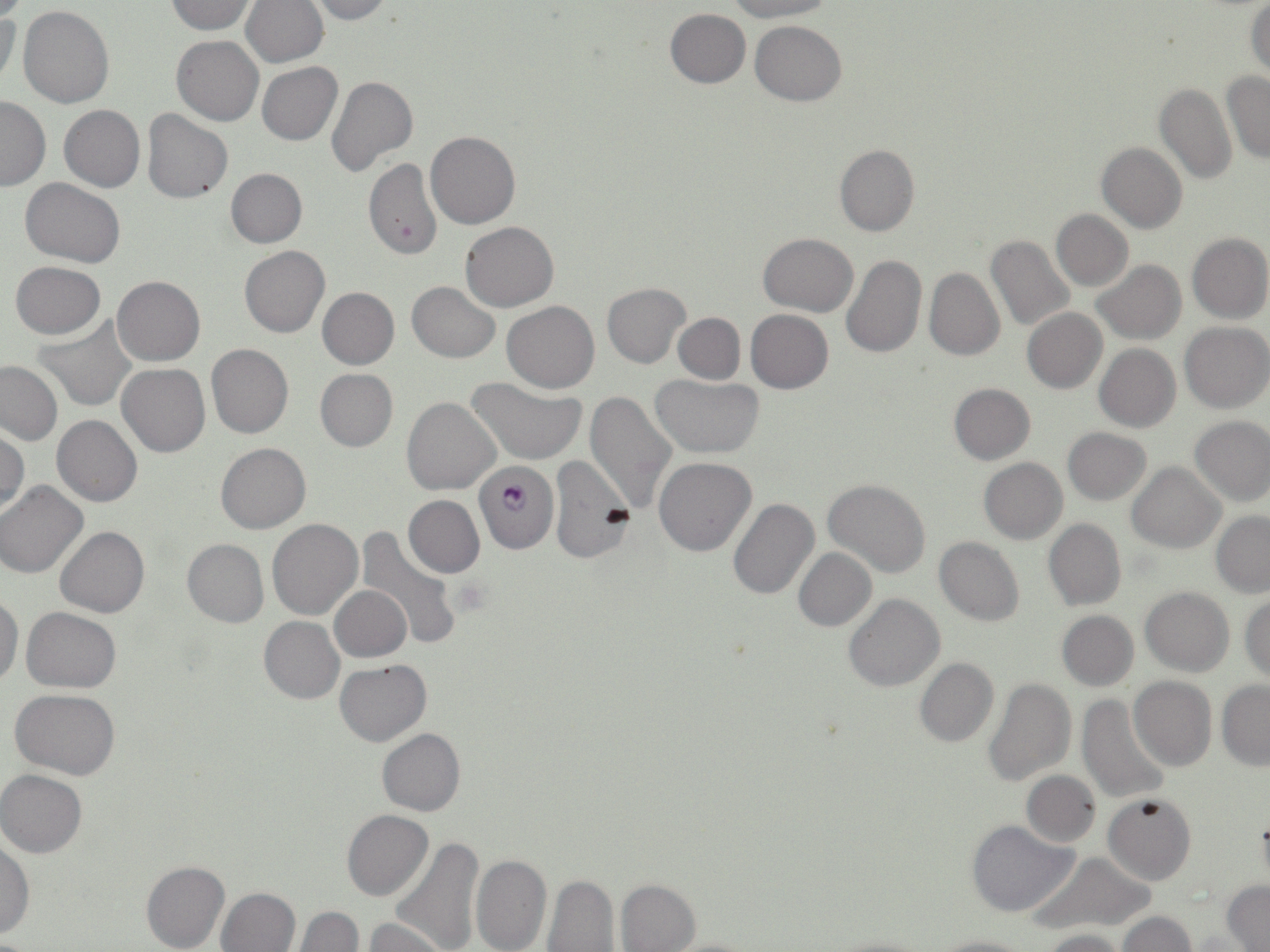 Approximate bounding boxes as [x1, y1, x2, y2] in pixels. Platelet locations: [453, 578, 493, 617]. Plasmodium falciparum-infected red blood cell locations: [478, 468, 560, 558]. Uninfected red blood cell locations: [242, 0, 328, 68], [302, 0, 393, 24], [727, 0, 837, 21], [163, 1, 259, 34], [1245, 1, 1269, 78], [0, 7, 20, 93], [19, 7, 115, 108], [665, 8, 750, 87], [751, 20, 847, 104], [172, 35, 264, 125], [256, 62, 343, 146], [1222, 71, 1270, 164], [327, 75, 417, 179], [1155, 82, 1237, 184], [0, 96, 50, 190], [59, 104, 145, 192], [142, 108, 232, 203], [425, 130, 521, 229], [1096, 141, 1188, 233], [834, 143, 919, 236], [364, 158, 441, 261], [226, 169, 306, 248], [20, 178, 125, 266], [1051, 209, 1132, 291], [461, 221, 558, 311], [1187, 232, 1269, 324], [758, 233, 858, 316], [985, 235, 1075, 330], [240, 245, 330, 338], [841, 255, 927, 359], [10, 261, 106, 339], [1091, 261, 1186, 344], [924, 267, 1004, 361], [113, 275, 206, 365], [407, 281, 500, 362], [602, 282, 690, 367], [317, 287, 399, 369], [501, 301, 600, 391], [1022, 307, 1107, 392], [746, 310, 833, 393], [673, 312, 745, 383], [33, 316, 138, 411], [1180, 321, 1270, 412], [1094, 343, 1181, 432], [206, 344, 293, 438], [0, 361, 62, 446], [117, 363, 210, 456], [315, 368, 398, 451], [651, 375, 765, 458], [467, 377, 588, 464], [948, 383, 1035, 464], [583, 393, 677, 514], [403, 397, 501, 496], [52, 416, 142, 506], [1189, 417, 1270, 506], [1, 427, 29, 514], [1063, 427, 1151, 505], [215, 443, 311, 533], [549, 455, 636, 563], [655, 456, 757, 556], [979, 459, 1067, 543], [1127, 463, 1225, 552], [824, 479, 931, 578], [0, 480, 88, 578], [404, 495, 484, 578], [727, 497, 820, 600], [1211, 511, 1270, 596], [267, 519, 363, 620], [1044, 519, 1126, 610], [55, 526, 149, 618], [356, 528, 464, 652], [934, 536, 1025, 626], [182, 539, 268, 627], [794, 548, 876, 631], [329, 585, 411, 661], [1140, 586, 1234, 676], [843, 593, 945, 692], [0, 594, 22, 689], [1241, 595, 1270, 683], [20, 607, 120, 692], [1058, 610, 1138, 690], [259, 616, 344, 704], [914, 658, 998, 748], [335, 659, 431, 746], [1129, 676, 1216, 771], [983, 678, 1077, 786], [1216, 681, 1270, 769], [10, 689, 121, 778], [1076, 695, 1172, 803], [377, 729, 465, 816], [1, 769, 87, 857], [1021, 770, 1100, 847], [1103, 793, 1196, 884], [1256, 805, 1270, 893], [342, 809, 433, 900], [965, 820, 1079, 916], [388, 837, 486, 952], [0, 839, 34, 938], [1030, 850, 1156, 936], [471, 853, 551, 952], [141, 860, 229, 952], [542, 875, 619, 951], [616, 879, 701, 951], [1222, 881, 1269, 951], [216, 887, 299, 952], [290, 907, 363, 952], [1118, 912, 1196, 952], [364, 918, 451, 952], [1037, 927, 1128, 952], [825, 933, 937, 952], [928, 934, 1032, 952], [661, 937, 762, 952]. Slide-level diagnosis: Plasmodium falciparum. Thin blood smear. Image is 1270×952 pixels. May-Grünwald-Giemsa stain. 1000x magnification. Single field of view. Light microscopy.